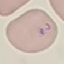
malaria status = parasitized
capture = smartphone camera at the microscope eyepiece
image type = cell patch, automatically extracted from a larger field of view and resized to 64 × 64 pixels
preparation = thin blood film
stain = Giemsa